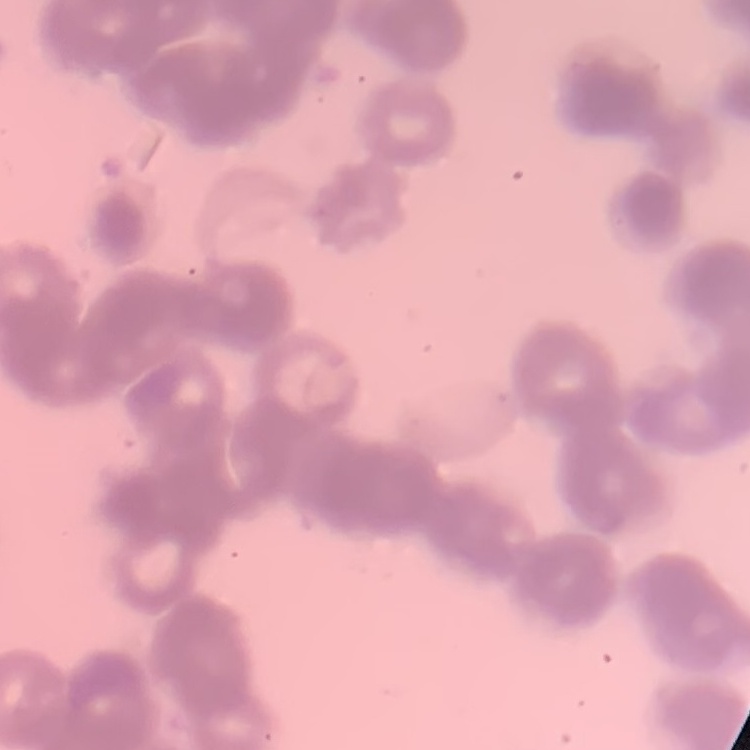
The red blood cells show rouleaux formation. Thin blood film. Stained with either Field's or Giemsa. Square crop of a larger photomicrograph.